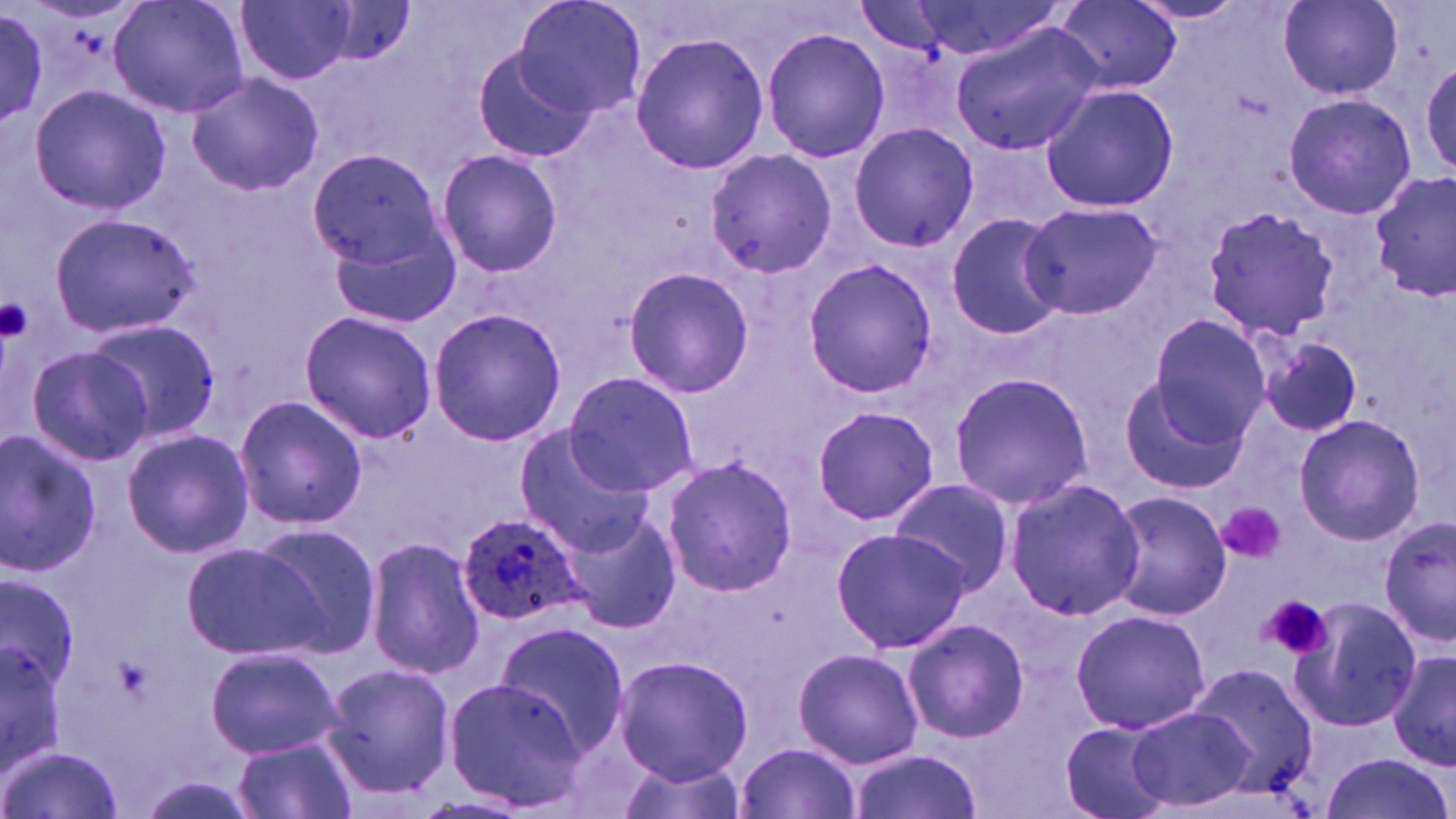
slide_level_diagnosis: Plasmodium ovale
magnification: 1000x
uninfected_red_blood_cell_locations: 'approximate bounding boxes as named x1/y1/x2/y2 corners in pixels: (x1=110, y1=0, x2=251, y2=118), (x1=237, y1=0, x2=358, y2=86), (x1=514, y1=0, x2=649, y2=119), (x1=879, y1=0, x2=1074, y2=63), (x1=1128, y1=0, x2=1249, y2=25), (x1=1053, y1=1, x2=1182, y2=94), (x1=1278, y1=1, x2=1403, y2=100), (x1=0, y1=10, x2=49, y2=129), (x1=950, y1=22, x2=1103, y2=157), (x1=764, y1=26, x2=888, y2=166), (x1=631, y1=33, x2=771, y2=174), (x1=470, y1=40, x2=595, y2=163), (x1=186, y1=72, x2=324, y2=197), (x1=28, y1=83, x2=173, y2=214), (x1=1039, y1=84, x2=1179, y2=212), (x1=1285, y1=93, x2=1418, y2=219), (x1=848, y1=122, x2=979, y2=253), (x1=307, y1=149, x2=445, y2=272), (x1=435, y1=149, x2=563, y2=278), (x1=702, y1=149, x2=836, y2=283), (x1=1369, y1=174, x2=1455, y2=302), (x1=1018, y1=200, x2=1164, y2=320), (x1=1205, y1=205, x2=1341, y2=337), (x1=944, y1=211, x2=1067, y2=342), (x1=49, y1=212, x2=198, y2=340), (x1=328, y1=221, x2=462, y2=328), (x1=801, y1=258, x2=939, y2=397), (x1=620, y1=267, x2=756, y2=397), (x1=428, y1=307, x2=566, y2=448), (x1=298, y1=310, x2=438, y2=445), (x1=1148, y1=316, x2=1273, y2=444), (x1=82, y1=317, x2=222, y2=447), (x1=1255, y1=331, x2=1365, y2=438), (x1=24, y1=343, x2=155, y2=466), (x1=561, y1=370, x2=699, y2=498), (x1=948, y1=373, x2=1096, y2=510), (x1=1121, y1=377, x2=1245, y2=494), (x1=231, y1=393, x2=369, y2=530), (x1=811, y1=405, x2=940, y2=527), (x1=1294, y1=416, x2=1424, y2=545), (x1=513, y1=425, x2=658, y2=553), (x1=121, y1=428, x2=255, y2=558), (x1=0, y1=429, x2=104, y2=579), (x1=660, y1=455, x2=798, y2=597), (x1=886, y1=478, x2=1017, y2=598), (x1=1000, y1=478, x2=1146, y2=622), (x1=1105, y1=490, x2=1232, y2=621), (x1=558, y1=507, x2=681, y2=635), (x1=1377, y1=514, x2=1456, y2=644), (x1=249, y1=523, x2=380, y2=653), (x1=828, y1=527, x2=970, y2=653), (x1=365, y1=536, x2=483, y2=681), (x1=185, y1=539, x2=333, y2=663), (x1=1, y1=576, x2=80, y2=695), (x1=1290, y1=597, x2=1423, y2=733), (x1=1069, y1=608, x2=1211, y2=735), (x1=903, y1=617, x2=1030, y2=744), (x1=492, y1=621, x2=629, y2=756), (x1=0, y1=629, x2=67, y2=776), (x1=205, y1=646, x2=344, y2=759), (x1=792, y1=647, x2=924, y2=768), (x1=1388, y1=647, x2=1456, y2=772), (x1=614, y1=655, x2=751, y2=784), (x1=1186, y1=661, x2=1318, y2=802), (x1=322, y1=663, x2=457, y2=797), (x1=441, y1=675, x2=590, y2=811), (x1=1126, y1=705, x2=1254, y2=811), (x1=1060, y1=721, x2=1174, y2=819), (x1=233, y1=736, x2=358, y2=819), (x1=737, y1=741, x2=863, y2=819), (x1=1, y1=743, x2=124, y2=819), (x1=848, y1=751, x2=985, y2=819), (x1=1319, y1=753, x2=1454, y2=819), (x1=610, y1=757, x2=751, y2=819)'
field_of_view: single
stain: May-Grünwald-Giemsa
platelet_locations: 'approximate bounding boxes as named x1/y1/x2/y2 corners in pixels: (x1=0, y1=297, x2=32, y2=345), (x1=1216, y1=502, x2=1285, y2=565), (x1=1259, y1=596, x2=1335, y2=664)'
modality: optical microscopy
plasmodium_ovale_infected_red_blood_cell_locations: 'approximate bounding boxes as named x1/y1/x2/y2 corners in pixels: (x1=457, y1=511, x2=586, y2=626)'
preparation: thin blood film
image_size: 1456×819 pixels